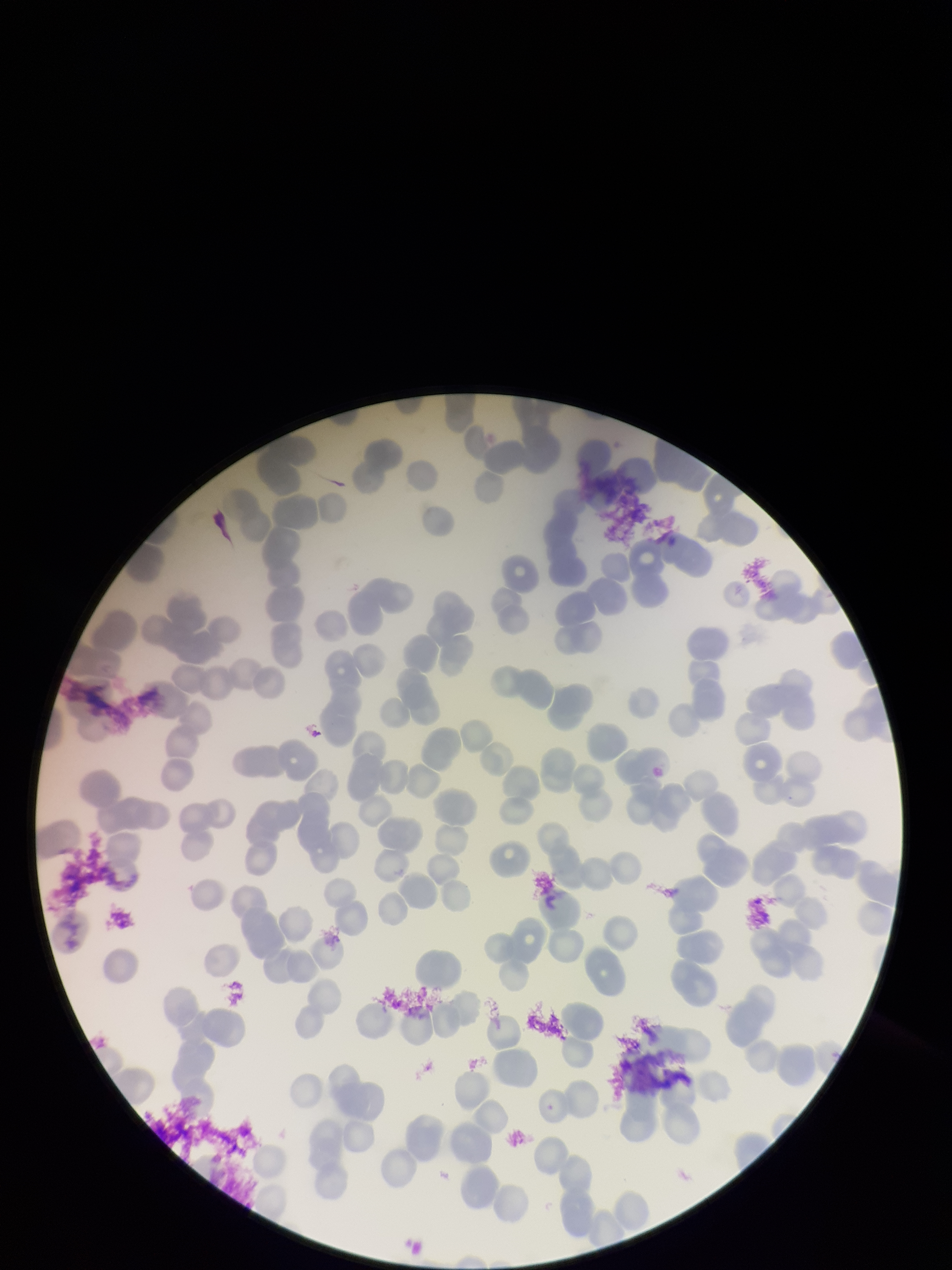
Parasitized red blood cells: none identified. Preparation: thin smear. Parasitized red blood cell count: 0. Species reported for this patient: Plasmodium falciparum. Patient malaria status: infected. Image is 952×1270 pixels. Photographed through the microscope eyepiece with a smartphone camera. One field from this slide. Red blood cell count: 137. Stained with Giemsa.